Identify the cell.
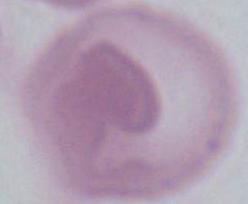

This is an erythrocyte.

Summary:
  - Modality: photomicrograph
  - Magnification: 1000x